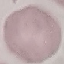 Result: negative for malaria parasites. Giemsa-stained preparation. Cell patch, automatically extracted from a larger field of view and resized to 64 × 64 pixels. Photographed with a smartphone camera at the microscope eyepiece. Thin smear of blood.